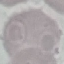

Result: no malaria parasites seen. Thin blood film. Cell patch, automatically extracted from a larger field of view and resized to 64 × 64 pixels. Giemsa-stained preparation. Acquired by smartphone through the microscope eyepiece.